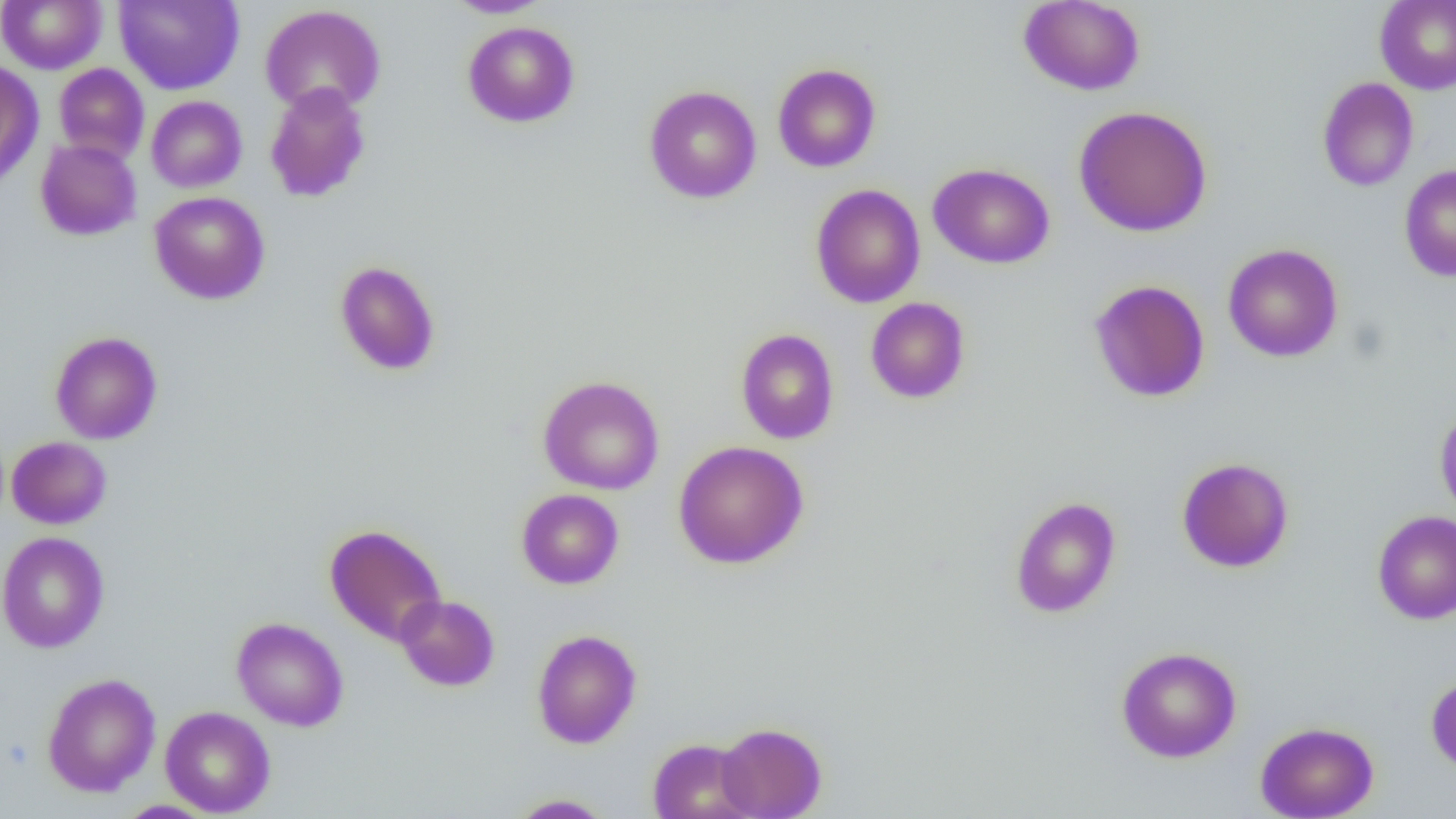 Approximate bounding boxes as (x1, y1, x2, y2) in pixels. Uninfected red blood cell locations: (445, 0, 553, 18), (1019, 0, 1145, 95), (0, 1, 107, 74), (114, 1, 244, 94), (1374, 1, 1456, 95), (259, 4, 387, 116), (462, 21, 580, 128), (0, 60, 44, 190), (53, 63, 149, 164), (773, 63, 881, 173), (1317, 77, 1419, 191), (264, 82, 372, 203), (644, 85, 761, 204), (146, 95, 247, 192), (1073, 105, 1212, 237), (35, 138, 142, 241), (927, 163, 1055, 269), (1399, 165, 1456, 282), (810, 183, 926, 309), (149, 191, 270, 304), (1223, 243, 1343, 362), (334, 260, 441, 375), (1088, 279, 1210, 402), (865, 297, 970, 403), (736, 328, 839, 444), (50, 331, 163, 445), (538, 375, 664, 495), (1434, 407, 1456, 521), (6, 436, 112, 529), (673, 440, 809, 569), (1177, 457, 1294, 572), (516, 489, 624, 589), (1009, 496, 1122, 618), (1372, 510, 1456, 625), (325, 523, 447, 646), (0, 531, 109, 653), (395, 594, 500, 691), (231, 616, 349, 732), (531, 629, 642, 748), (1116, 646, 1241, 763), (42, 673, 161, 797), (1426, 673, 1456, 774), (159, 706, 275, 817), (1255, 721, 1379, 818), (717, 722, 827, 818), (648, 737, 756, 819), (508, 794, 615, 818), (115, 800, 218, 818). Slide-level diagnosis: negative for blood parasites. One field of a larger specimen. Thin blood smear. Captured at 1000x magnification. Optical microscopy. Image is 1456×819 pixels.